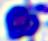

Summary:
  - Magnification: 400x
  - Identification: white blood cell
  - Modality: micrograph